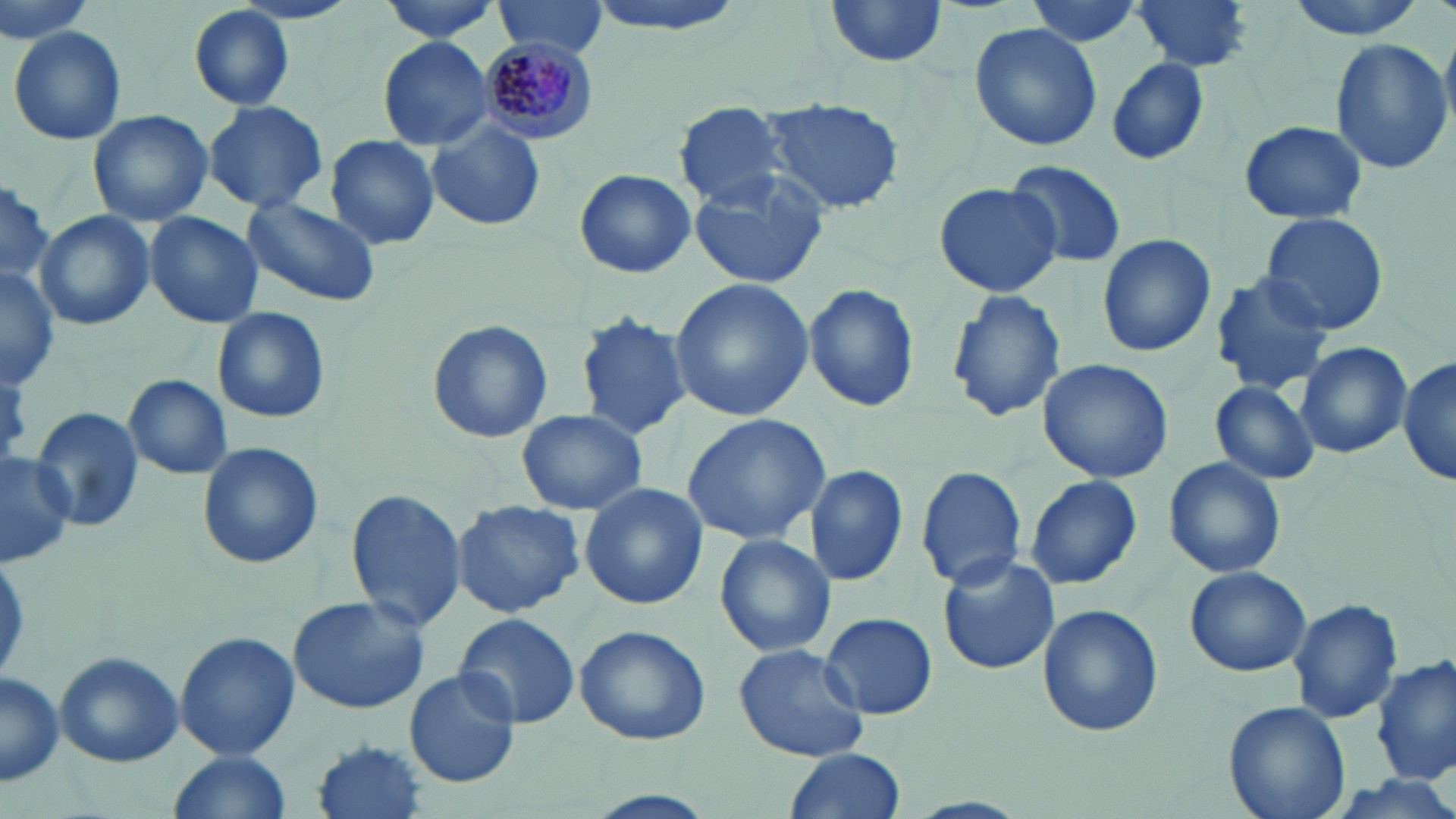
slide_level_diagnosis: Plasmodium malariae
preparation: thin blood smear
plasmodium_malariae_infected_red_blood_cell_locations: 'approximate bounding boxes as (x1,y1)-(x2,y2) corner pairs in pixels: (474,34)-(601,145)'
magnification: 1000x
uninfected_red_blood_cell_locations: 'approximate bounding boxes as (x1,y1)-(x2,y2) corner pairs in pixels: (376,0)-(511,43), (823,0)-(949,70), (1024,0)-(1144,47), (1130,0)-(1254,74), (1282,0)-(1432,41), (494,2)-(609,59), (188,5)-(296,112), (967,22)-(1101,151), (8,25)-(127,146), (376,34)-(498,152), (1328,37)-(1453,177), (1103,57)-(1213,167), (759,97)-(904,216), (201,100)-(329,211), (675,105)-(791,209), (86,108)-(215,227), (1239,120)-(1370,225), (427,121)-(546,233), (326,135)-(441,249), (1003,157)-(1126,270), (574,169)-(696,278), (686,169)-(832,288), (0,176)-(53,289), (932,180)-(1062,297), (243,194)-(380,307), (144,211)-(264,329), (1259,211)-(1390,335), (36,212)-(155,331), (1097,233)-(1216,358), (0,264)-(61,390), (1207,272)-(1336,394), (667,278)-(813,423), (804,282)-(921,414), (945,287)-(1066,422), (211,306)-(332,424), (574,312)-(695,439), (425,319)-(554,444), (1296,341)-(1411,460), (1399,354)-(1456,486), (1036,358)-(1173,484), (124,374)-(233,478), (1209,379)-(1320,486), (30,406)-(144,534), (517,408)-(647,516), (679,413)-(830,546), (196,442)-(324,570), (0,450)-(79,566), (1163,457)-(1286,579), (804,463)-(910,587), (915,465)-(1028,590), (1024,476)-(1143,591), (578,480)-(708,612), (344,487)-(468,633), (449,499)-(586,618), (714,533)-(837,659), (936,552)-(1061,676), (1184,566)-(1311,677), (287,594)-(429,715), (1286,597)-(1402,724), (1036,605)-(1163,737), (819,611)-(938,720), (452,613)-(581,729), (575,624)-(711,746), (173,631)-(299,761), (734,642)-(870,762), (53,650)-(185,767), (1373,653)-(1455,785), (404,668)-(522,788), (0,670)-(64,787), (1224,698)-(1351,819), (311,738)-(429,819), (783,749)-(906,819), (168,751)-(292,817)'
modality: optical microscopy
stain: May-Grünwald-Giemsa
image_size: 1456×819 pixels
field_of_view: single